Give the extent of all Plasmodium malariae-infected red blood cells.
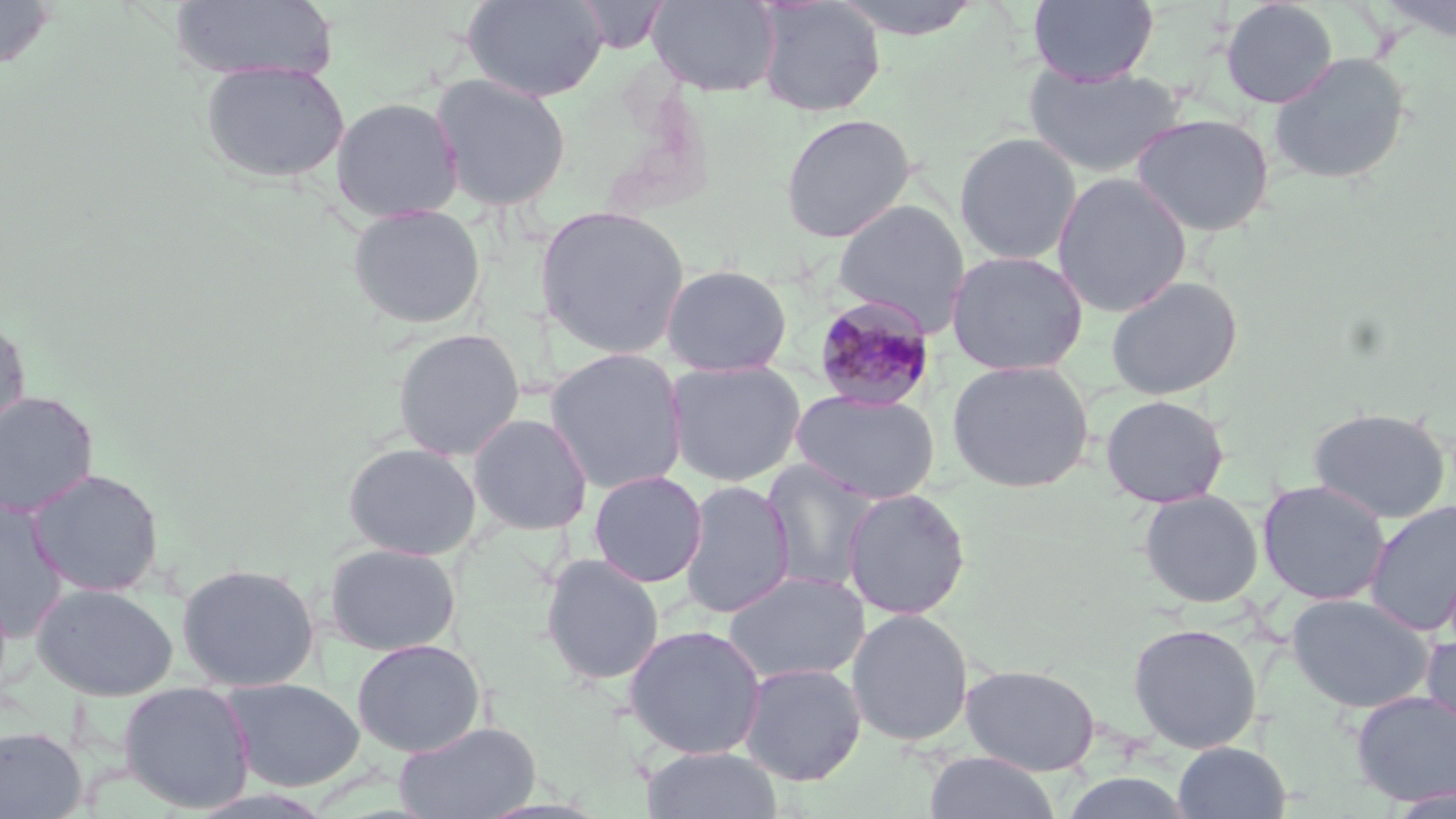
Approximate bounding boxes as (x1, y1, x2, y2) in pixels.
Plasmodium malariae-infected red blood cells: (812, 295, 937, 412).

slide-level diagnosis = Plasmodium malariae
magnification = 1000x
modality = light microscopy
preparation = thin blood smear
image size = 1456×819 pixels
stain = May-Grünwald-Giemsa
uninfected red blood cell locations = approximate bounding boxes as (x1, y1, x2, y2) in pixels: (0, 0, 56, 73), (462, 0, 609, 102), (646, 0, 782, 97), (754, 0, 886, 117), (826, 0, 988, 40), (1028, 0, 1159, 86), (1220, 0, 1338, 109), (1376, 0, 1456, 44), (169, 1, 338, 83), (1268, 51, 1412, 185), (199, 59, 351, 185), (1023, 62, 1185, 177), (430, 73, 572, 211), (330, 96, 465, 223), (780, 112, 917, 243), (1131, 112, 1275, 236), (953, 131, 1083, 266), (1052, 172, 1192, 317), (833, 199, 971, 330), (347, 204, 487, 329), (534, 205, 691, 359), (946, 250, 1088, 375), (660, 264, 793, 377), (1106, 275, 1243, 400), (0, 313, 31, 444), (391, 327, 526, 460), (545, 347, 689, 493), (666, 359, 806, 487), (946, 359, 1094, 493), (791, 389, 942, 504), (0, 391, 99, 518), (1100, 394, 1230, 508), (1307, 407, 1452, 524), (467, 412, 594, 535), (342, 441, 482, 560), (760, 458, 884, 594), (27, 468, 165, 597), (588, 470, 708, 587), (679, 479, 796, 619), (1257, 479, 1391, 605), (841, 487, 972, 620), (1138, 489, 1264, 607), (0, 497, 70, 642), (1364, 500, 1456, 636), (324, 542, 462, 656), (539, 554, 665, 686), (176, 562, 320, 692), (722, 571, 870, 684), (31, 582, 179, 701), (1285, 593, 1435, 713), (845, 608, 974, 747), (1127, 621, 1263, 753), (623, 624, 768, 760), (1420, 632, 1456, 740), (351, 638, 486, 757), (738, 662, 867, 785), (961, 664, 1101, 776), (220, 677, 366, 791), (118, 681, 256, 813), (1350, 690, 1456, 806), (394, 720, 541, 819), (0, 726, 88, 818), (1173, 741, 1292, 818), (642, 745, 784, 819), (923, 751, 1060, 819), (1058, 771, 1197, 819)
field of view = single